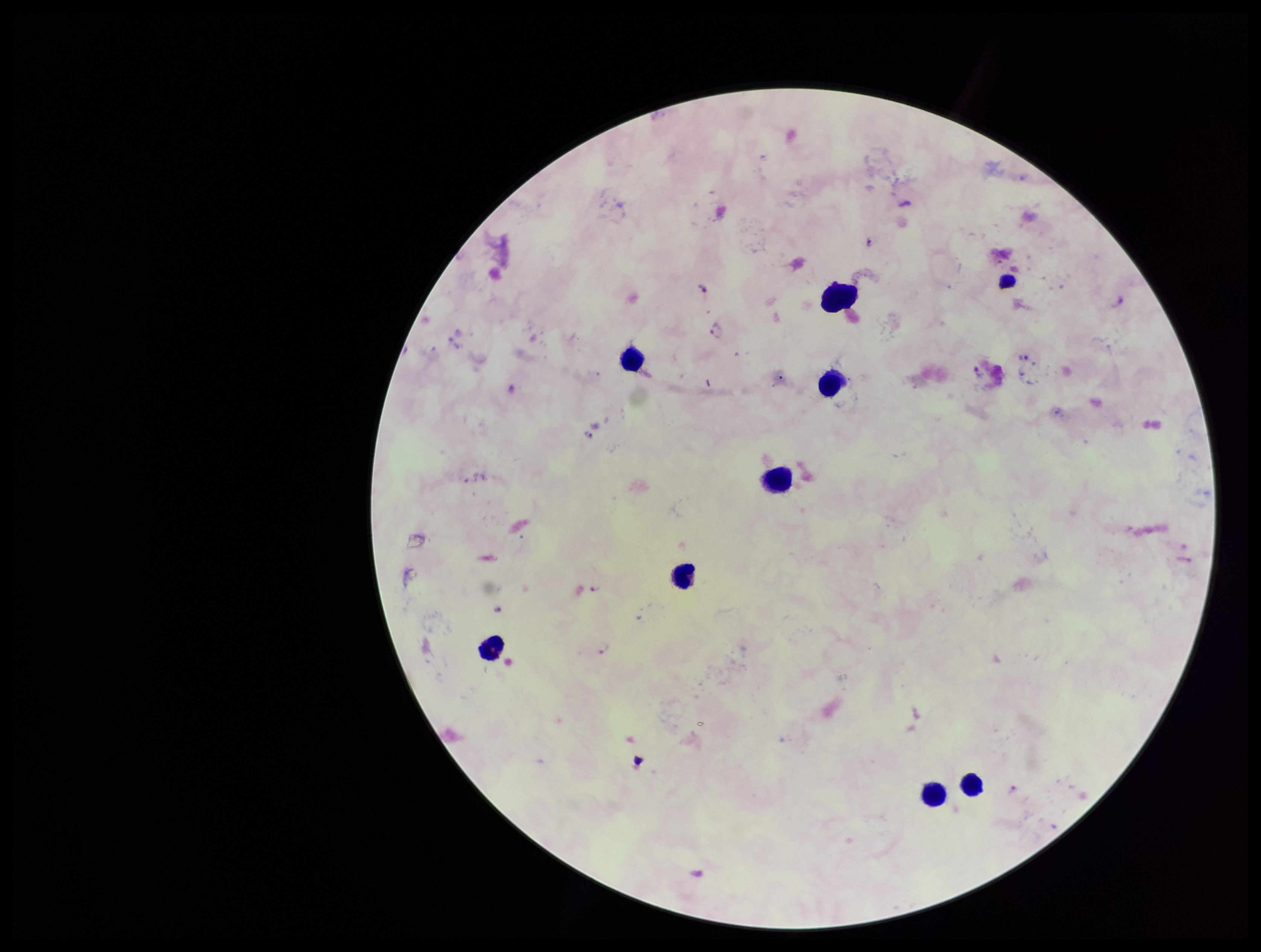

plasmodium_parasites: seen
species_reported_for_this_patient: Plasmodium falciparum
leukocyte_count: 9
preparation: thick smear
stain: Giemsa
patient_malaria_status: infected
field_of_view: single
capture: smartphone photograph through the microscope eyepiece
parasite_count: 5
image_size: 1261×952 pixels